Give the preparation type.
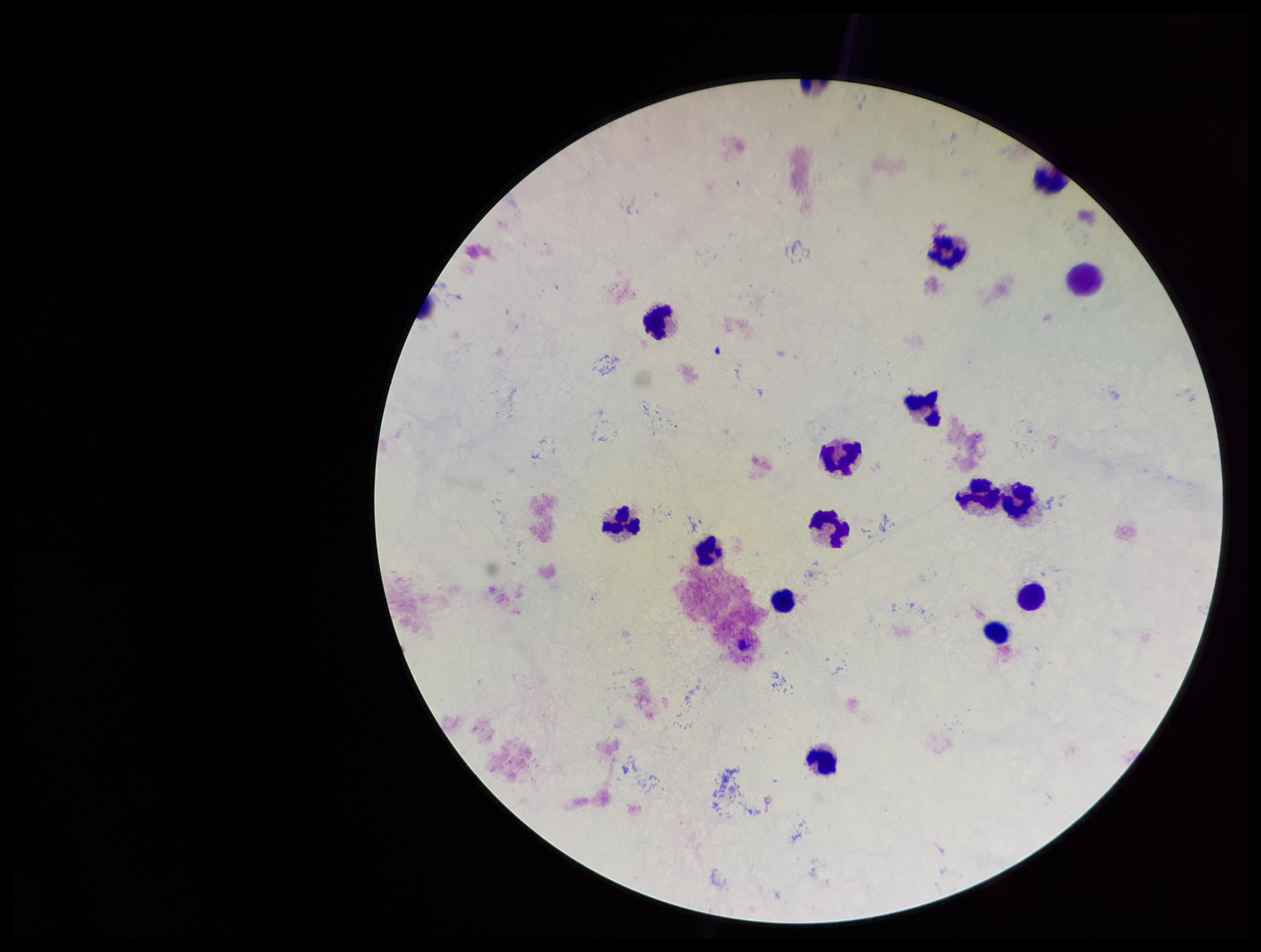

Thick.

Summary:
  - Capture: smartphone photograph through the microscope eyepiece
  - Leukocyte count: 16
  - Stain: Giemsa
  - Field of view: one from this slide
  - Patient malaria status: negative
  - Plasmodium parasites: none seen
  - Image size: 1261×952 pixels
  - Parasite count: 0